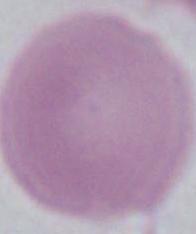 1000x magnification. Micrograph. An erythrocyte is seen.